Locate every Trypanosoma brucei.
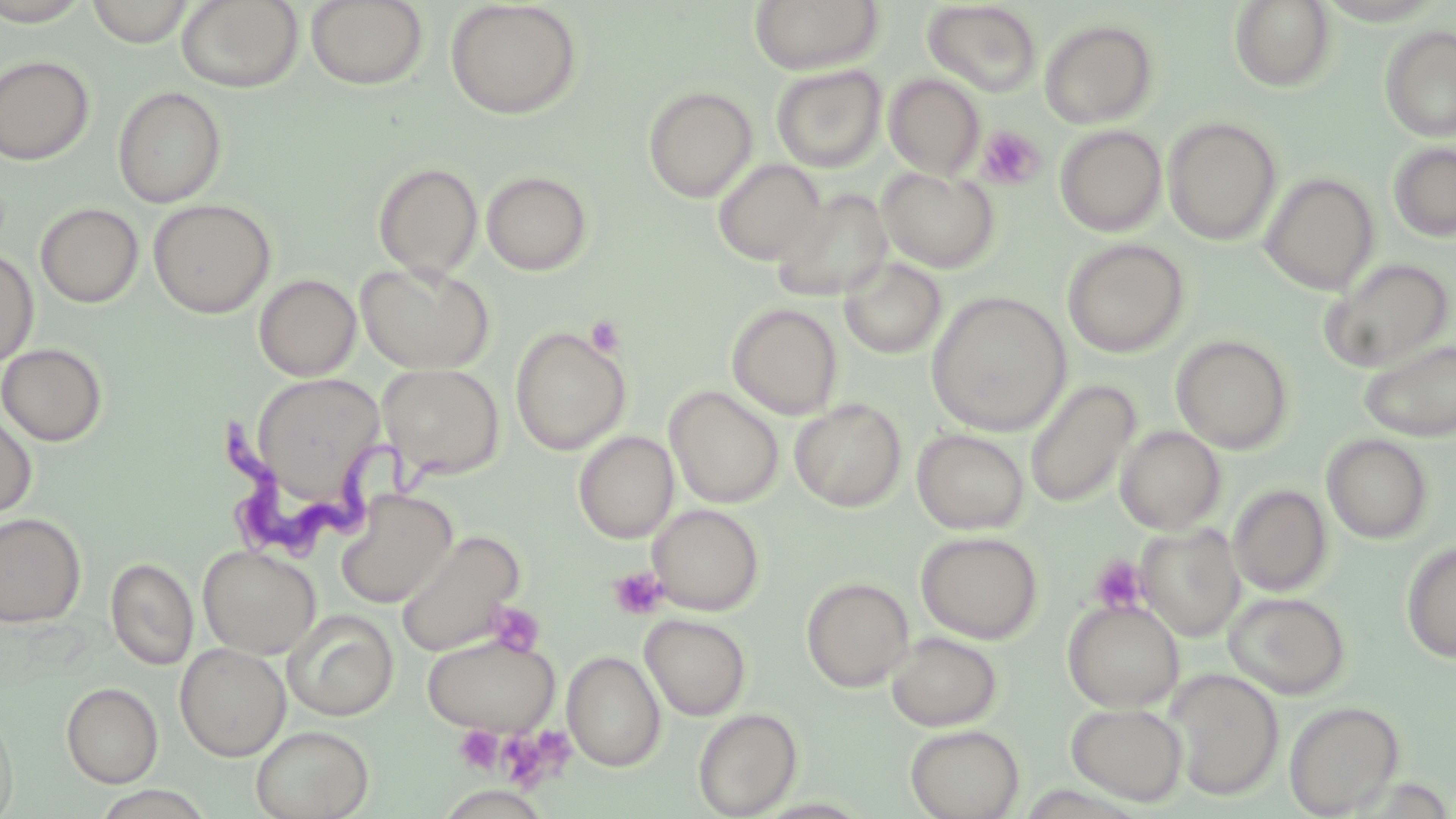
Approximate bounding boxes as (x1,y1)-(x2,y2) corner pairs in pixels.
Trypanosoma brucei: (225,411)-(444,562).

Summary:
  - Uninfected red blood cell locations: (0,0)-(93,25), (177,0)-(303,93), (307,0)-(429,90), (749,0)-(884,74), (1229,0)-(1335,92), (87,1)-(194,46), (445,1)-(582,120), (923,2)-(1042,96), (1039,20)-(1158,128), (1380,25)-(1456,141), (0,55)-(95,165), (771,65)-(886,172), (884,73)-(985,178), (642,85)-(757,202), (113,86)-(227,208), (1164,117)-(1281,244), (1055,126)-(1166,236), (1389,142)-(1456,242), (713,158)-(826,266), (373,161)-(484,280), (877,167)-(1000,272), (481,170)-(594,276), (1261,173)-(1378,294), (771,188)-(894,303), (148,199)-(276,318), (36,203)-(144,308), (1062,239)-(1189,357), (0,248)-(39,367), (838,257)-(947,359), (1318,257)-(1454,374), (355,261)-(495,375), (254,274)-(361,381), (927,290)-(1071,436), (727,303)-(843,420), (510,326)-(631,455), (1171,335)-(1294,454), (1359,338)-(1456,442), (0,343)-(107,446), (378,363)-(505,479), (249,372)-(388,508), (1025,379)-(1141,507), (665,386)-(784,508), (789,399)-(906,512), (0,410)-(37,520), (1115,425)-(1225,534), (912,429)-(1029,534), (573,431)-(678,543), (1322,433)-(1433,543), (1228,484)-(1332,596), (335,489)-(457,608), (647,504)-(764,615), (0,512)-(86,628), (1136,523)-(1246,641), (396,530)-(526,656), (916,530)-(1043,644), (1401,541)-(1456,662), (198,544)-(322,659), (106,557)-(198,670), (801,576)-(915,692), (1224,591)-(1351,699), (1062,598)-(1184,712), (283,610)-(399,721), (640,614)-(751,720), (885,631)-(1002,731), (422,633)-(560,735), (175,643)-(291,760), (561,651)-(666,772), (1166,668)-(1285,799), (61,682)-(163,787), (1283,700)-(1404,817), (1066,702)-(1188,805), (0,707)-(18,819), (692,707)-(802,818), (905,724)-(1024,819), (251,725)-(374,819)
  - Platelet locations: (977,125)-(1045,189), (585,314)-(627,358), (1090,554)-(1147,614), (608,567)-(668,621), (487,602)-(547,657), (454,725)-(503,773), (499,728)-(572,794)
  - Slide-level diagnosis: Trypanosoma brucei
  - Field of view: one of a larger specimen
  - Stain: May-Grünwald-Giemsa
  - Preparation: thin blood film
  - Magnification: 1000x
  - Image size: 1456×819 pixels
  - Modality: optical microscopy